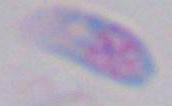

Summary:
  - Identification: Toxoplasma gondii
  - Modality: photomicrograph
  - Magnification: 1000x